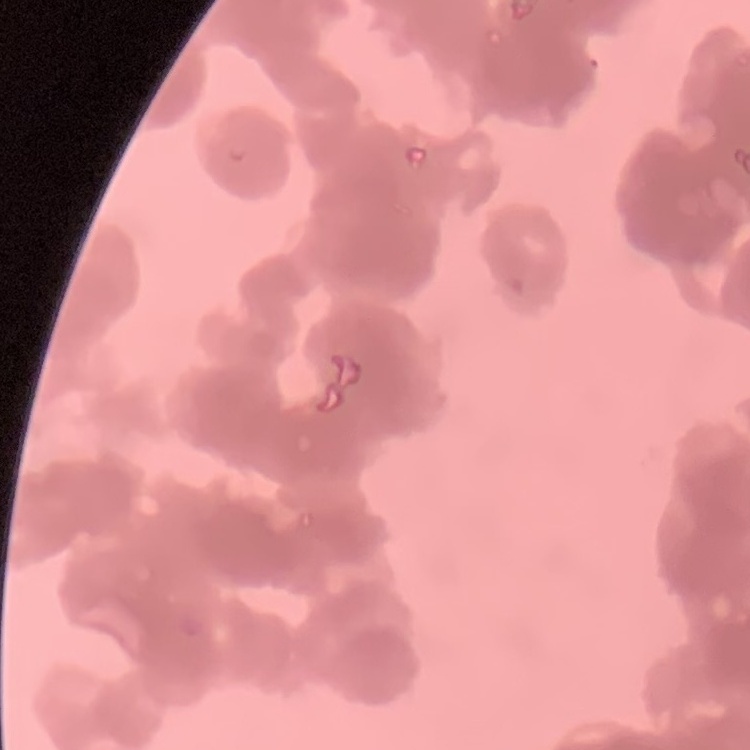
erythrocyte_morphology: rouleaux formation
preparation: thin blood smear
stain: Field's or Giemsa
image_type: one tile cut from a larger photomicrograph